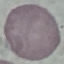
Result: no malaria parasites detected. Giemsa-stained preparation. Cell patch, automatically extracted from a larger field of view and resized to 64 × 64 pixels. Thin smear of blood. Photographed with a smartphone camera at the microscope eyepiece.